Evaluate for parasitized red blood cells.
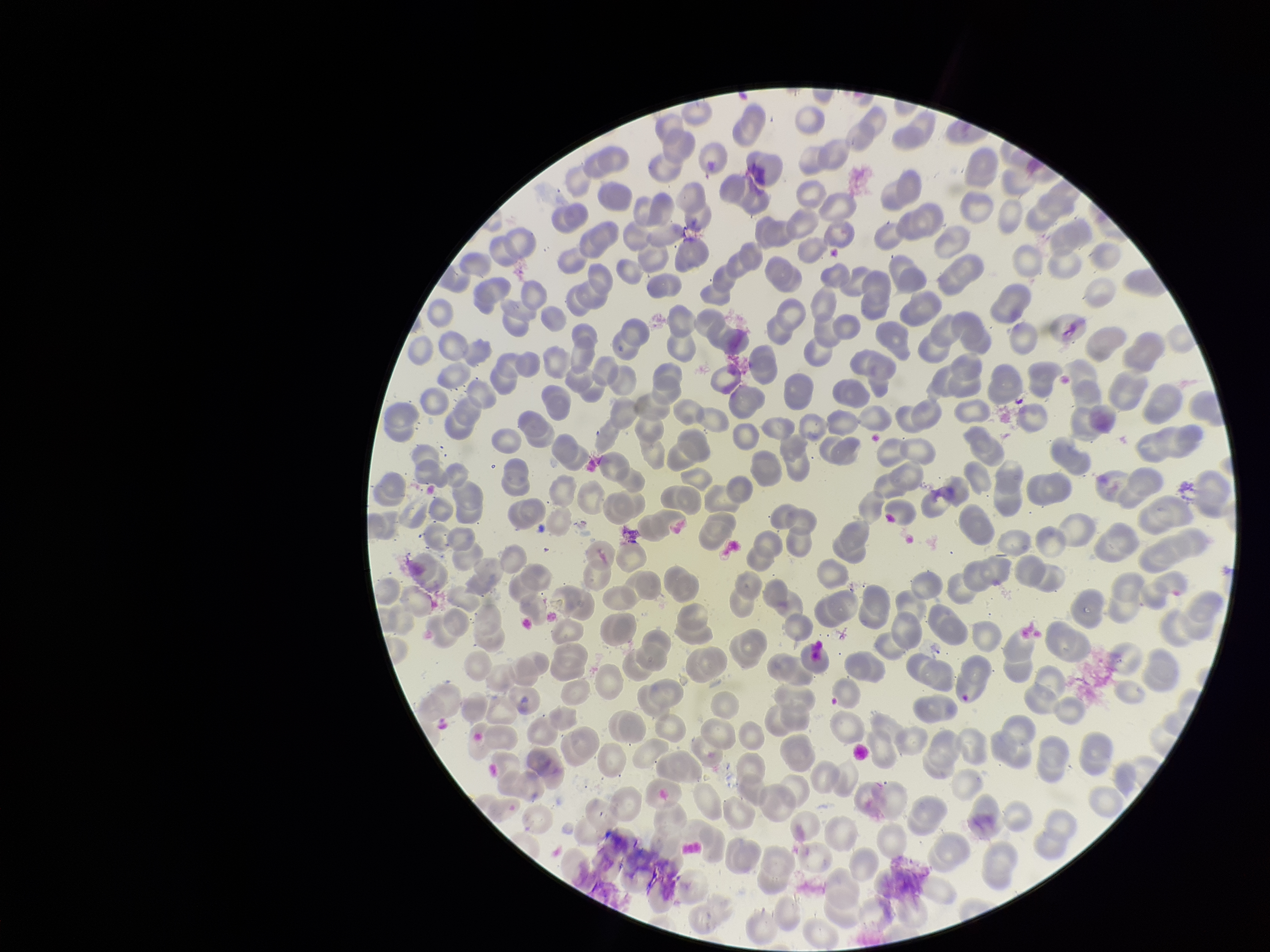
None identified.

Summary:
  - Patient malaria status: negative
  - Parasitized red blood cell count: 0
  - Preparation: thin smear
  - Stain: Giemsa
  - Field of view: one from this slide
  - Capture: smartphone photograph through the microscope eyepiece
  - Red blood cell count: 290
  - Image size: 1270×952 pixels